Name the parasite shown.
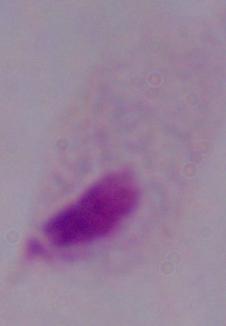
A trichomonad.

1000x magnification. Photomicrograph.